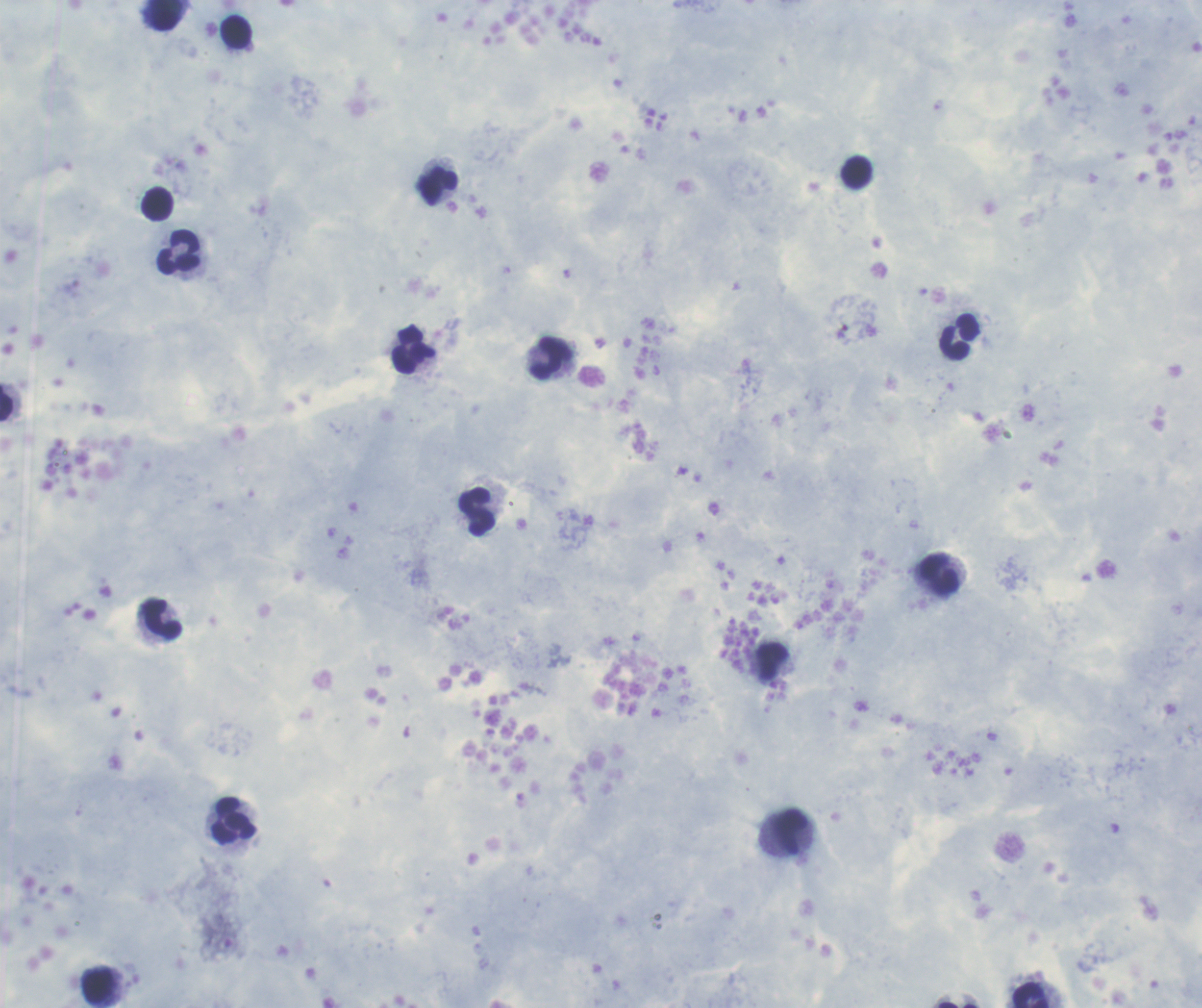
{
  "leukocyte_locations": "approximate centers as (x, y) in pixels: (166, 15), (236, 32), (856, 172), (438, 186), (157, 203), (179, 251), (959, 337), (413, 351), (550, 358), (7, 403), (476, 511), (939, 575), (163, 620), (772, 661), (234, 820), (791, 832), (97, 986), (1032, 995)",
  "field_of_view": "single",
  "image_size": "1202×1008 pixels",
  "background_quality": "satisfactory",
  "context": "previously used in a real diagnosis",
  "coloration_quality": "good",
  "preparation": "thick blood smear",
  "magnification": "100x",
  "result": "no Plasmodium parasites detected",
  "stain": "Romanowsky"
}